Give the position of every Plasmodium parasite visible.
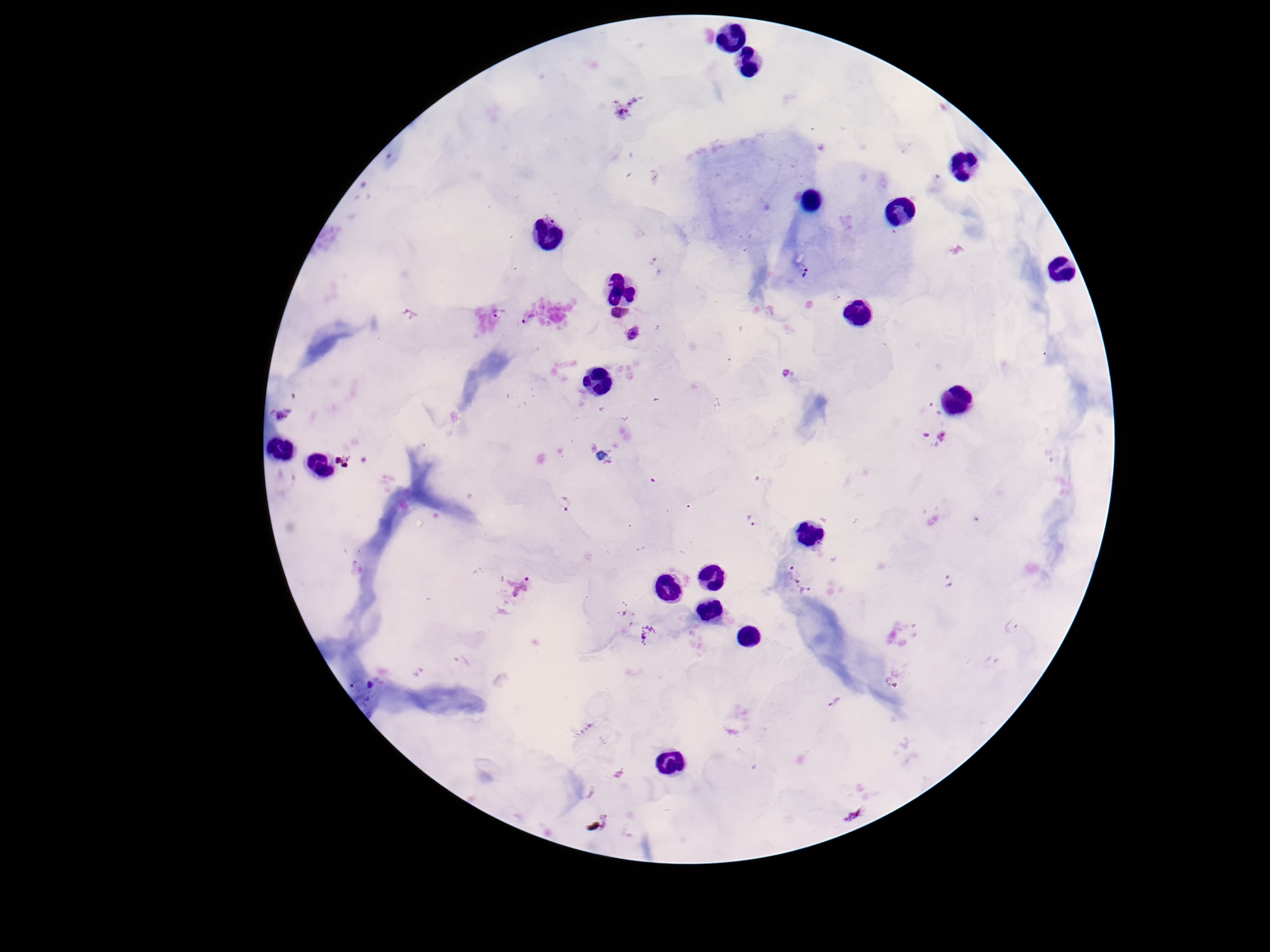
Approximate centers as [x, y] in pixels.
Plasmodium parasites: [658, 267], [805, 273], [619, 312], [499, 313], [529, 320], [634, 335], [790, 372], [935, 408], [933, 437], [564, 502], [752, 521], [792, 573], [949, 582], [519, 587], [807, 592], [1014, 626].

Thick blood smear. One field from this slide. Smartphone photograph taken through the microscope eyepiece. Patient malaria status: positive. Image is 1270×952 pixels. Giemsa-stained preparation. 100x magnification.